Locate and identify every blood parasite.
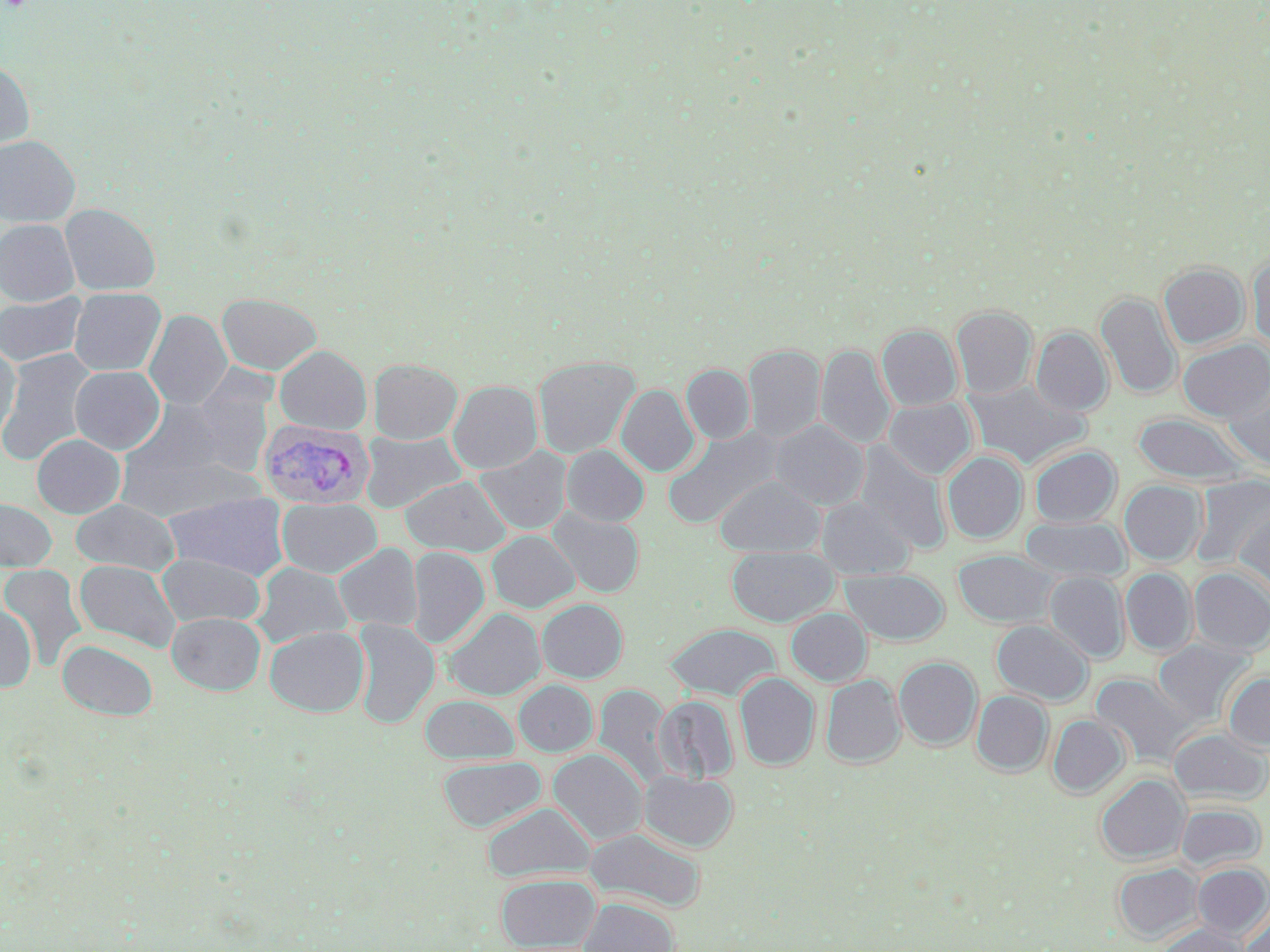

Approximate bounding boxes as named x1/y1/x2/y2 corners in pixels.
Plasmodium vivax-infected red blood cells: (x1=260, y1=421, x2=374, y2=509).
No Plasmodium falciparum, Plasmodium ovale, Plasmodium malariae, Babesia divergens, or Trypanosoma brucei observed.

slide-level diagnosis = Plasmodium vivax
magnification = 1000x
image size = 1270×952 pixels
field of view = single
stain = May-Grünwald-Giemsa
preparation = thin blood smear
modality = optical microscopy
uninfected red blood cell locations = approximate bounding boxes as named x1/y1/x2/y2 corners in pixels: (x1=0, y1=61, x2=34, y2=158), (x1=0, y1=135, x2=80, y2=227), (x1=60, y1=204, x2=160, y2=295), (x1=0, y1=219, x2=80, y2=306), (x1=1248, y1=254, x2=1270, y2=350), (x1=1158, y1=262, x2=1249, y2=349), (x1=69, y1=287, x2=166, y2=376), (x1=0, y1=292, x2=87, y2=368), (x1=1095, y1=292, x2=1181, y2=399), (x1=217, y1=293, x2=321, y2=375), (x1=951, y1=305, x2=1037, y2=399), (x1=144, y1=310, x2=232, y2=410), (x1=877, y1=325, x2=962, y2=411), (x1=1031, y1=327, x2=1112, y2=416), (x1=1178, y1=339, x2=1270, y2=422), (x1=0, y1=341, x2=21, y2=441), (x1=743, y1=344, x2=825, y2=444), (x1=815, y1=344, x2=896, y2=450), (x1=274, y1=345, x2=372, y2=434), (x1=0, y1=349, x2=97, y2=467), (x1=533, y1=356, x2=640, y2=459), (x1=368, y1=358, x2=462, y2=444), (x1=681, y1=364, x2=755, y2=444), (x1=70, y1=366, x2=165, y2=454), (x1=1223, y1=376, x2=1270, y2=471), (x1=963, y1=379, x2=1089, y2=469), (x1=448, y1=380, x2=542, y2=474), (x1=617, y1=384, x2=699, y2=477), (x1=129, y1=394, x2=268, y2=484), (x1=883, y1=398, x2=976, y2=479), (x1=1132, y1=413, x2=1254, y2=485), (x1=770, y1=420, x2=869, y2=510), (x1=662, y1=426, x2=784, y2=530), (x1=359, y1=431, x2=467, y2=513), (x1=771, y1=432, x2=950, y2=531), (x1=31, y1=433, x2=125, y2=518), (x1=853, y1=441, x2=952, y2=552), (x1=561, y1=445, x2=649, y2=526), (x1=475, y1=446, x2=573, y2=536), (x1=1028, y1=446, x2=1121, y2=527), (x1=942, y1=451, x2=1027, y2=544), (x1=1193, y1=474, x2=1270, y2=570), (x1=400, y1=475, x2=511, y2=556), (x1=715, y1=475, x2=824, y2=557), (x1=1120, y1=480, x2=1206, y2=566), (x1=164, y1=491, x2=290, y2=580), (x1=817, y1=497, x2=914, y2=579), (x1=277, y1=498, x2=382, y2=578), (x1=0, y1=499, x2=57, y2=572), (x1=71, y1=499, x2=179, y2=575), (x1=548, y1=507, x2=645, y2=598), (x1=1234, y1=508, x2=1270, y2=601), (x1=1019, y1=517, x2=1130, y2=583), (x1=487, y1=530, x2=579, y2=612), (x1=334, y1=543, x2=422, y2=632), (x1=408, y1=546, x2=489, y2=648), (x1=727, y1=546, x2=837, y2=627), (x1=953, y1=550, x2=1059, y2=628), (x1=156, y1=552, x2=266, y2=627), (x1=74, y1=559, x2=181, y2=653), (x1=251, y1=562, x2=353, y2=647), (x1=1, y1=565, x2=88, y2=671), (x1=1188, y1=566, x2=1270, y2=656), (x1=1120, y1=568, x2=1196, y2=656), (x1=842, y1=569, x2=949, y2=645), (x1=1045, y1=571, x2=1129, y2=663), (x1=537, y1=599, x2=627, y2=683), (x1=0, y1=604, x2=37, y2=692), (x1=443, y1=607, x2=545, y2=700), (x1=786, y1=608, x2=871, y2=686), (x1=167, y1=612, x2=265, y2=695), (x1=351, y1=619, x2=439, y2=729), (x1=992, y1=620, x2=1092, y2=704), (x1=664, y1=623, x2=780, y2=700), (x1=264, y1=625, x2=369, y2=717), (x1=57, y1=639, x2=158, y2=720), (x1=1152, y1=639, x2=1253, y2=727), (x1=894, y1=657, x2=982, y2=750), (x1=735, y1=673, x2=819, y2=770), (x1=1223, y1=673, x2=1270, y2=750), (x1=821, y1=674, x2=906, y2=768), (x1=1090, y1=674, x2=1195, y2=768), (x1=514, y1=680, x2=597, y2=756), (x1=593, y1=684, x2=672, y2=787), (x1=971, y1=691, x2=1052, y2=777), (x1=653, y1=694, x2=738, y2=783), (x1=421, y1=695, x2=519, y2=764), (x1=1048, y1=714, x2=1129, y2=798), (x1=1169, y1=727, x2=1270, y2=804), (x1=548, y1=749, x2=647, y2=846), (x1=438, y1=756, x2=546, y2=832), (x1=640, y1=770, x2=737, y2=852), (x1=1095, y1=774, x2=1189, y2=864), (x1=483, y1=802, x2=594, y2=882), (x1=1175, y1=802, x2=1265, y2=872), (x1=585, y1=826, x2=706, y2=913), (x1=1113, y1=862, x2=1202, y2=942), (x1=1193, y1=863, x2=1270, y2=938), (x1=497, y1=873, x2=600, y2=951), (x1=580, y1=898, x2=678, y2=952), (x1=1240, y1=907, x2=1270, y2=952), (x1=1156, y1=924, x2=1249, y2=952)